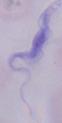
1000x magnification. Photomicrograph. A trypanosome is shown.